Assess for malaria.
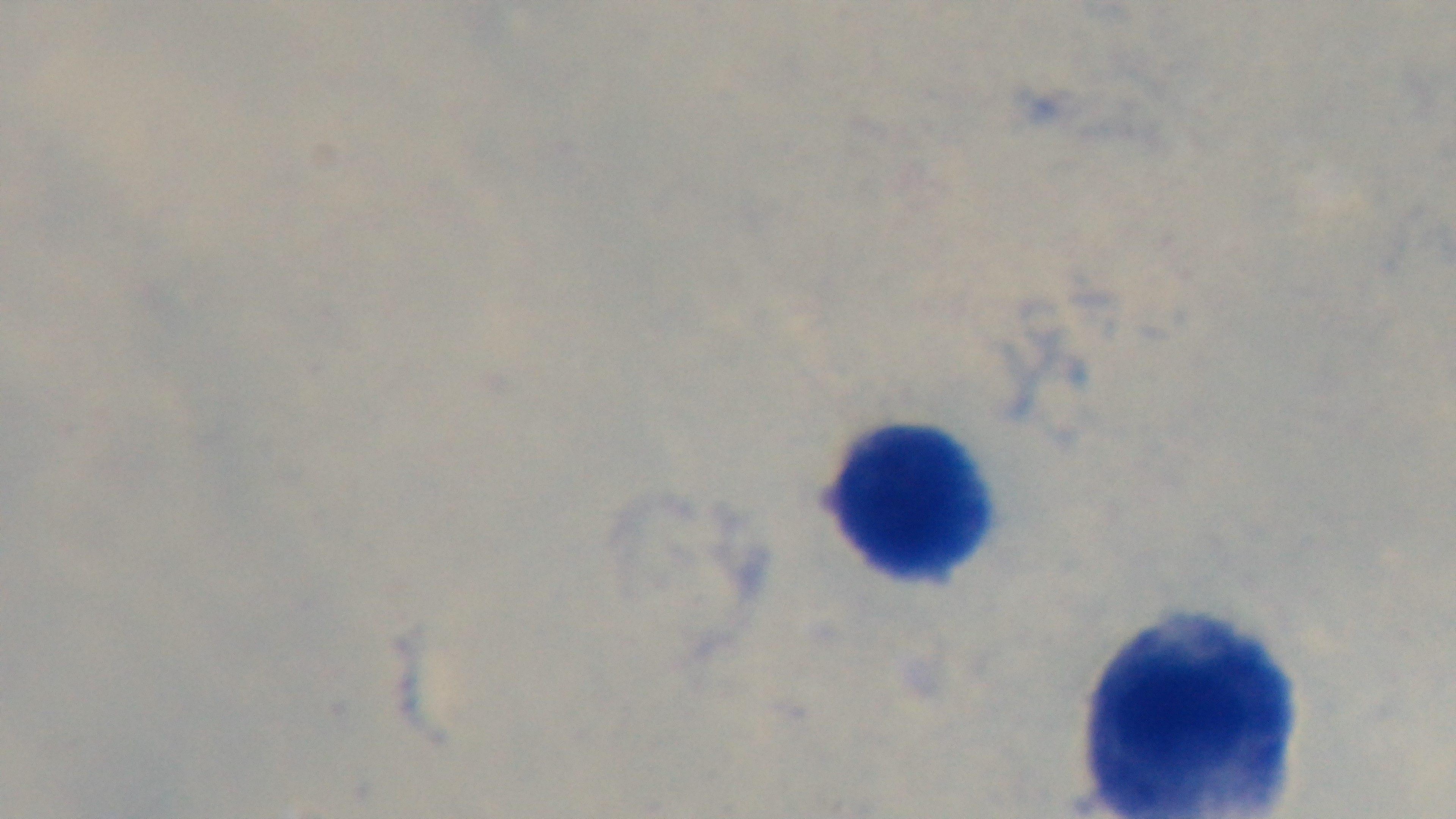
Uninfected.

Oil-immersion objective, 100x. Captured with a mounted 4K digital camera. Light microscopy. Single field of view. Preparation: thick. Giemsa-stained.